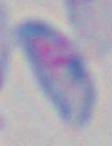

Summary:
  - Modality: micrograph
  - Identification: Toxoplasma gondii
  - Magnification: 1000x